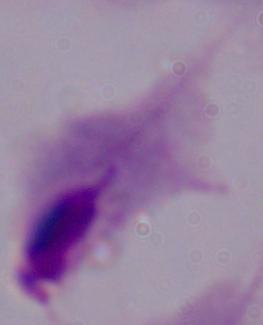

Photomicrograph. Captured at 1000x magnification. A trichomonad is shown.